Locate platelets.
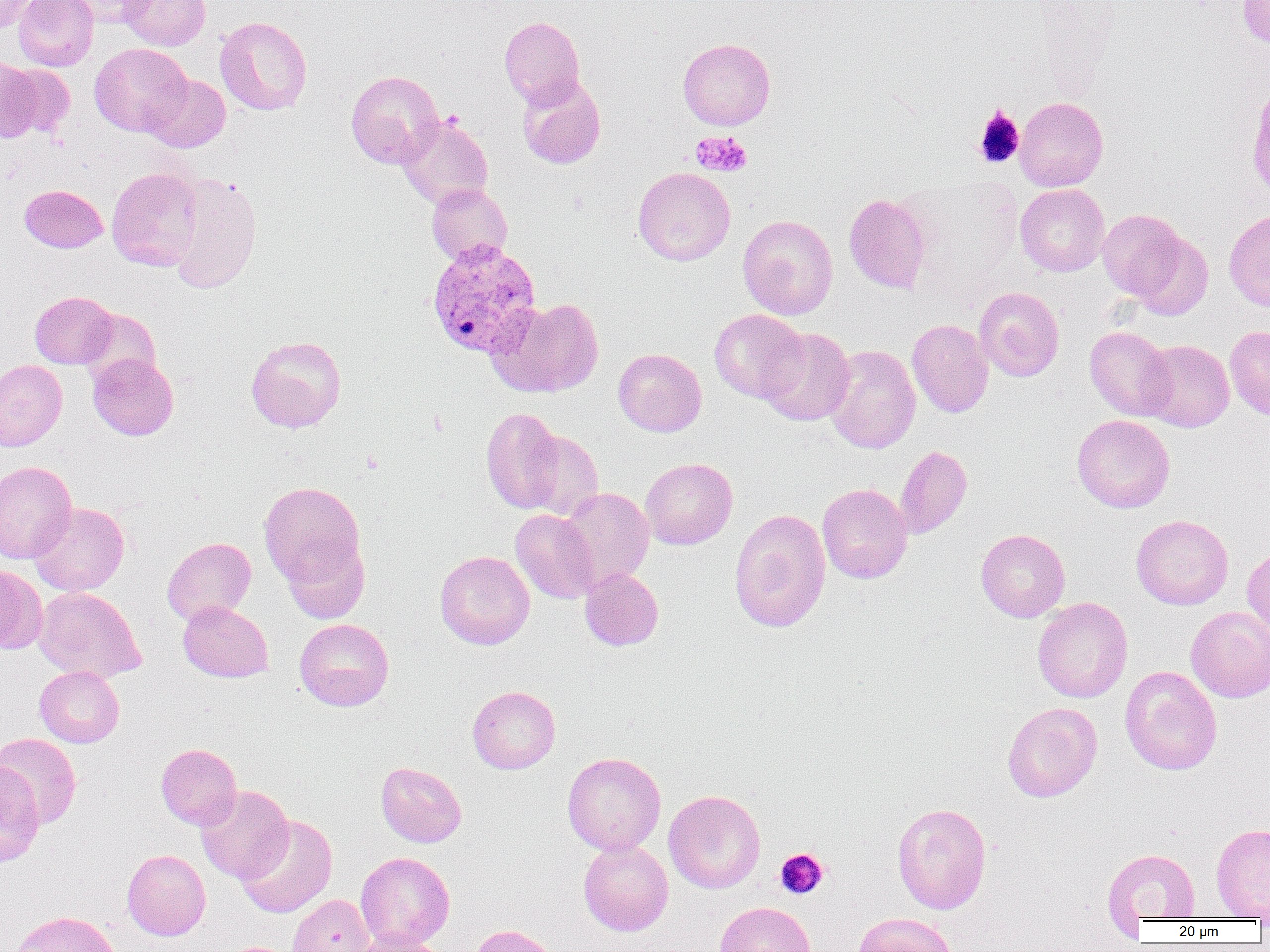
Approximate bounding boxes as (x1, y1, x2, y2) in pixels.
Platelets: (973, 105, 1025, 169), (690, 131, 752, 177), (775, 848, 829, 900).

Summary:
  - Plasmodium vivax-infected red blood cell locations: (426, 239, 541, 359)
  - Uninfected red blood cell locations: (0, 0, 38, 34), (13, 0, 98, 71), (64, 0, 154, 28), (118, 0, 210, 50), (1238, 1, 1270, 48), (214, 16, 312, 115), (499, 16, 585, 107), (677, 38, 775, 130), (89, 42, 191, 137), (2, 62, 74, 137), (345, 70, 443, 168), (143, 74, 231, 152), (517, 75, 606, 169), (1015, 97, 1109, 191), (397, 114, 493, 210), (633, 166, 735, 266), (106, 167, 203, 271), (168, 174, 263, 294), (426, 184, 513, 266), (1015, 184, 1110, 277), (20, 185, 108, 253), (844, 193, 933, 294), (1097, 208, 1196, 306), (1224, 208, 1270, 313), (737, 214, 839, 320), (974, 286, 1064, 382), (29, 291, 117, 369), (487, 297, 604, 398), (79, 308, 161, 387), (709, 309, 808, 402), (907, 319, 994, 418), (1225, 325, 1270, 419), (1085, 326, 1176, 421), (757, 327, 855, 426), (246, 335, 346, 432), (1139, 339, 1234, 432), (824, 344, 921, 454), (613, 348, 707, 437), (87, 354, 179, 440), (0, 360, 67, 451), (480, 406, 564, 514), (1072, 414, 1175, 513), (521, 429, 604, 522), (894, 445, 972, 538), (640, 457, 737, 550), (0, 460, 77, 564), (259, 482, 366, 589), (817, 483, 913, 584), (560, 487, 654, 587), (29, 502, 129, 595), (510, 508, 601, 604), (729, 508, 830, 632), (1131, 514, 1233, 610), (975, 529, 1070, 622), (162, 537, 257, 625), (282, 537, 370, 624), (1242, 546, 1270, 640), (434, 550, 535, 650), (0, 564, 47, 655), (580, 567, 664, 650), (35, 586, 145, 682), (1033, 597, 1133, 703), (178, 601, 274, 682), (1186, 606, 1270, 702), (294, 618, 394, 711), (34, 666, 124, 747), (1120, 666, 1222, 775), (467, 685, 560, 774), (1002, 701, 1103, 802), (0, 733, 82, 828), (155, 743, 242, 830), (562, 752, 666, 856), (0, 759, 45, 868), (376, 761, 467, 848), (195, 785, 293, 883), (664, 790, 765, 893), (892, 802, 992, 914), (235, 814, 338, 918), (1211, 822, 1270, 920), (578, 839, 673, 936), (1102, 848, 1200, 922), (122, 849, 211, 940), (355, 852, 455, 950), (287, 894, 375, 952), (715, 901, 815, 952), (9, 910, 121, 952), (853, 913, 957, 952), (468, 924, 561, 952), (347, 932, 447, 952)
  - Slide-level diagnosis: Plasmodium vivax
  - Field of view: single
  - Preparation: thin blood smear
  - Modality: light microscopy
  - Magnification: 1000x
  - Image size: 1270×952 pixels